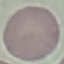

Malaria status: uninfected. Giemsa stain. Cell patch, automatically extracted from a larger field of view and resized to 64 × 64 pixels. Thin blood smear. Photographed with a smartphone camera at the microscope eyepiece.